Assess the morphology of the red blood cells.
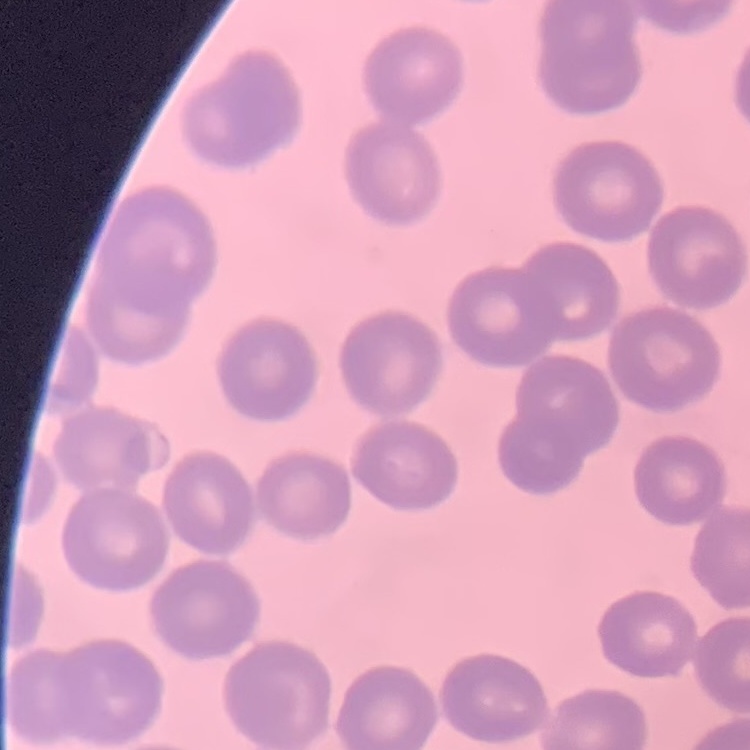
No rouleaux formation.

Summary:
  - Preparation: thin blood smear
  - Image type: square crop of a larger photomicrograph
  - Stain: Field's or Giemsa